Assess this cell for malaria.
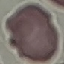
It is uninfected.

Summary:
  - Capture: smartphone camera at the microscope eyepiece
  - Preparation: thin blood smear
  - Stain: Giemsa
  - Image type: cell patch, automatically extracted from a larger field of view and resized to 64 × 64 pixels